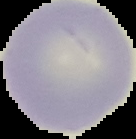

image size = 136×139 pixels
preparation = thin blood film
image type = segmented cell region with the area outside set to black
result = no malaria parasites seen